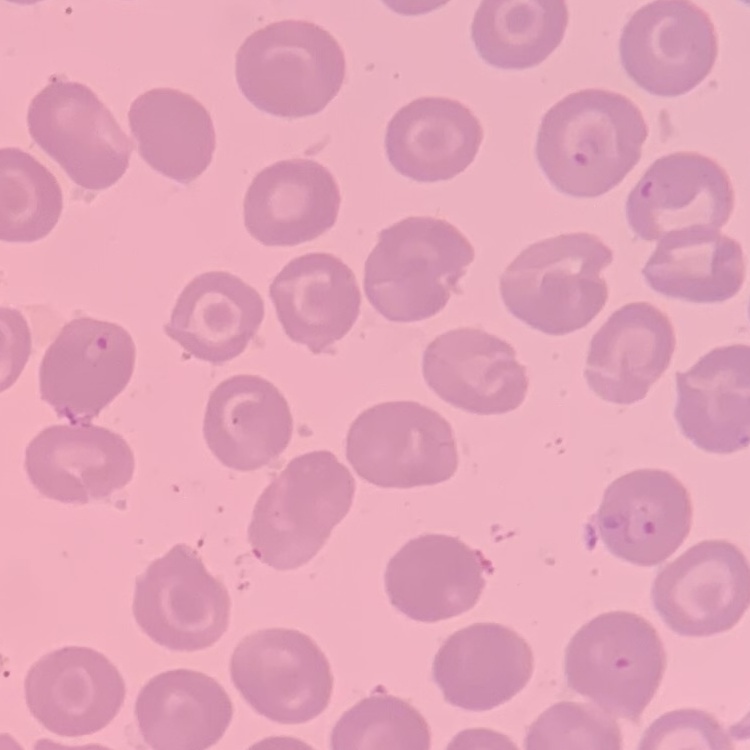

erythrocyte morphology = no rouleaux formation
image type = one tile cut from a larger photomicrograph
stain = Field's or Giemsa
preparation = thin peripheral smear